Outline each blood parasite and name the species.
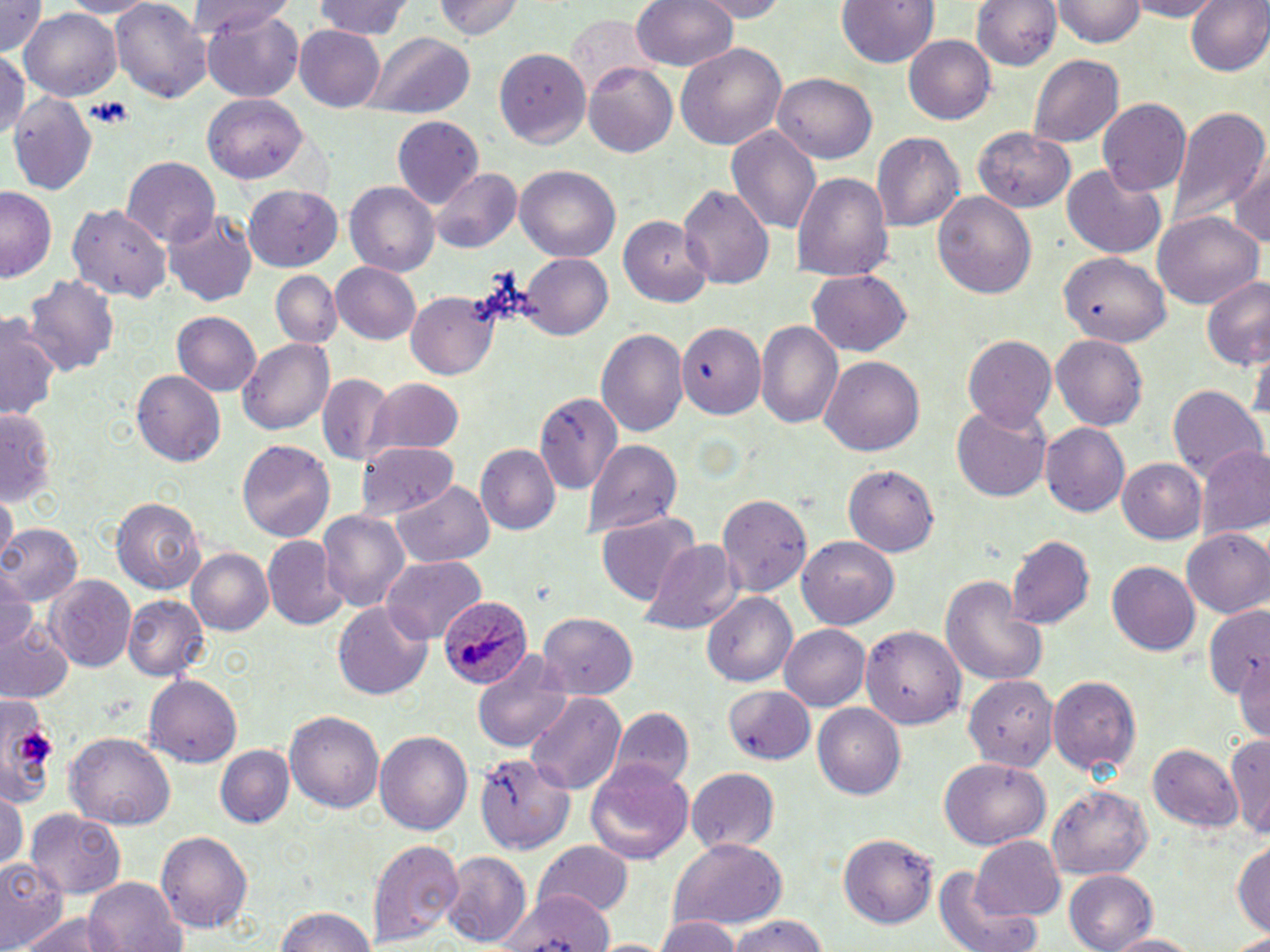

Approximate bounding boxes as named x1/y1/x2/y2 corners in pixels.
Plasmodium ovale-infected red blood cells: (x1=437, y1=598, x2=531, y2=691).
No Plasmodium falciparum, Plasmodium malariae, Plasmodium vivax, Babesia divergens, or Trypanosoma brucei observed.

slide-level diagnosis = Plasmodium ovale
modality = light microscopy
stain = May-Grünwald-Giemsa
platelet locations = approximate bounding boxes as named x1/y1/x2/y2 corners in pixels: (x1=83, y1=98, x2=133, y2=127), (x1=18, y1=729, x2=57, y2=764)
field of view = single
uninfected red blood cell locations = approximate bounding boxes as named x1/y1/x2/y2 corners in pixels: (x1=1, y1=0, x2=49, y2=57), (x1=111, y1=0, x2=214, y2=104), (x1=314, y1=0, x2=417, y2=40), (x1=431, y1=0, x2=522, y2=42), (x1=631, y1=0, x2=739, y2=73), (x1=690, y1=0, x2=794, y2=20), (x1=969, y1=0, x2=1062, y2=71), (x1=1055, y1=0, x2=1145, y2=47), (x1=1125, y1=0, x2=1220, y2=20), (x1=1185, y1=0, x2=1270, y2=79), (x1=836, y1=1, x2=940, y2=69), (x1=187, y1=3, x2=298, y2=44), (x1=202, y1=6, x2=304, y2=102), (x1=19, y1=9, x2=121, y2=103), (x1=563, y1=16, x2=654, y2=101), (x1=295, y1=26, x2=385, y2=110), (x1=366, y1=33, x2=473, y2=120), (x1=904, y1=37, x2=996, y2=123), (x1=677, y1=41, x2=787, y2=151), (x1=494, y1=47, x2=593, y2=146), (x1=1028, y1=52, x2=1124, y2=148), (x1=0, y1=53, x2=28, y2=137), (x1=582, y1=62, x2=678, y2=156), (x1=771, y1=74, x2=877, y2=164), (x1=8, y1=91, x2=100, y2=199), (x1=205, y1=95, x2=307, y2=182), (x1=1097, y1=97, x2=1192, y2=196), (x1=1167, y1=105, x2=1268, y2=230), (x1=391, y1=115, x2=484, y2=212), (x1=973, y1=127, x2=1074, y2=213), (x1=726, y1=128, x2=822, y2=237), (x1=872, y1=130, x2=964, y2=232), (x1=1228, y1=154, x2=1270, y2=250), (x1=122, y1=156, x2=217, y2=245), (x1=1061, y1=164, x2=1168, y2=259), (x1=515, y1=166, x2=620, y2=262), (x1=430, y1=168, x2=522, y2=254), (x1=791, y1=171, x2=892, y2=282), (x1=344, y1=182, x2=438, y2=277), (x1=245, y1=184, x2=343, y2=271), (x1=678, y1=184, x2=774, y2=291), (x1=1, y1=188, x2=55, y2=282), (x1=932, y1=191, x2=1036, y2=299), (x1=69, y1=202, x2=172, y2=304), (x1=165, y1=210, x2=256, y2=307), (x1=620, y1=214, x2=713, y2=305), (x1=1155, y1=214, x2=1262, y2=309), (x1=520, y1=253, x2=613, y2=339), (x1=1060, y1=253, x2=1169, y2=342), (x1=330, y1=262, x2=422, y2=344), (x1=807, y1=268, x2=911, y2=356), (x1=25, y1=271, x2=120, y2=380), (x1=273, y1=271, x2=340, y2=346), (x1=1200, y1=274, x2=1269, y2=371), (x1=408, y1=294, x2=496, y2=377), (x1=1, y1=312, x2=59, y2=423), (x1=170, y1=312, x2=261, y2=398), (x1=757, y1=321, x2=844, y2=430), (x1=678, y1=323, x2=765, y2=421), (x1=597, y1=327, x2=688, y2=436), (x1=962, y1=333, x2=1057, y2=430), (x1=1050, y1=335, x2=1148, y2=430), (x1=237, y1=337, x2=336, y2=435), (x1=820, y1=354, x2=926, y2=458), (x1=132, y1=371, x2=226, y2=466), (x1=317, y1=372, x2=391, y2=467), (x1=369, y1=379, x2=465, y2=456), (x1=1166, y1=382, x2=1266, y2=485), (x1=534, y1=387, x2=624, y2=493), (x1=953, y1=406, x2=1051, y2=502), (x1=0, y1=407, x2=55, y2=507), (x1=1041, y1=423, x2=1130, y2=518), (x1=237, y1=439, x2=335, y2=543), (x1=584, y1=441, x2=681, y2=539), (x1=356, y1=442, x2=460, y2=521), (x1=1196, y1=443, x2=1270, y2=539), (x1=474, y1=444, x2=559, y2=536), (x1=1118, y1=458, x2=1208, y2=545), (x1=842, y1=463, x2=941, y2=557), (x1=393, y1=483, x2=494, y2=566), (x1=716, y1=491, x2=814, y2=596), (x1=2, y1=494, x2=17, y2=558), (x1=112, y1=495, x2=206, y2=594), (x1=318, y1=509, x2=410, y2=611), (x1=596, y1=511, x2=701, y2=607), (x1=0, y1=524, x2=82, y2=606), (x1=1182, y1=529, x2=1270, y2=617), (x1=263, y1=535, x2=347, y2=629), (x1=1006, y1=535, x2=1095, y2=629), (x1=641, y1=536, x2=740, y2=632), (x1=799, y1=536, x2=899, y2=632), (x1=187, y1=548, x2=272, y2=635), (x1=381, y1=556, x2=485, y2=643), (x1=1107, y1=562, x2=1199, y2=657), (x1=0, y1=570, x2=37, y2=652), (x1=941, y1=572, x2=1047, y2=690), (x1=46, y1=576, x2=136, y2=673), (x1=123, y1=594, x2=208, y2=680), (x1=703, y1=594, x2=797, y2=686), (x1=334, y1=602, x2=433, y2=699), (x1=1204, y1=605, x2=1268, y2=710), (x1=540, y1=615, x2=637, y2=697), (x1=0, y1=619, x2=73, y2=703), (x1=858, y1=622, x2=967, y2=727), (x1=779, y1=624, x2=870, y2=711), (x1=472, y1=653, x2=576, y2=752), (x1=1233, y1=654, x2=1269, y2=746), (x1=961, y1=671, x2=1059, y2=776), (x1=143, y1=674, x2=244, y2=768), (x1=1046, y1=674, x2=1141, y2=776), (x1=724, y1=682, x2=814, y2=762), (x1=0, y1=693, x2=60, y2=800), (x1=527, y1=693, x2=625, y2=792), (x1=812, y1=702, x2=906, y2=800), (x1=286, y1=709, x2=385, y2=813), (x1=607, y1=711, x2=694, y2=795), (x1=1226, y1=729, x2=1270, y2=838), (x1=375, y1=730, x2=472, y2=837), (x1=64, y1=733, x2=175, y2=829), (x1=1147, y1=742, x2=1241, y2=831), (x1=217, y1=747, x2=294, y2=828), (x1=475, y1=750, x2=574, y2=854), (x1=584, y1=757, x2=695, y2=865), (x1=939, y1=757, x2=1049, y2=852), (x1=685, y1=767, x2=780, y2=853), (x1=1048, y1=786, x2=1154, y2=878), (x1=0, y1=791, x2=27, y2=874), (x1=24, y1=810, x2=123, y2=895), (x1=156, y1=830, x2=254, y2=934), (x1=836, y1=833, x2=938, y2=929), (x1=970, y1=835, x2=1066, y2=921), (x1=1233, y1=835, x2=1270, y2=939), (x1=368, y1=837, x2=464, y2=945), (x1=669, y1=838, x2=788, y2=931), (x1=535, y1=842, x2=633, y2=920), (x1=444, y1=853, x2=532, y2=945), (x1=0, y1=857, x2=65, y2=948), (x1=926, y1=869, x2=1046, y2=952), (x1=1063, y1=869, x2=1158, y2=951), (x1=83, y1=877, x2=185, y2=951), (x1=498, y1=890, x2=617, y2=952), (x1=273, y1=903, x2=380, y2=952), (x1=13, y1=912, x2=133, y2=952), (x1=655, y1=916, x2=739, y2=952), (x1=725, y1=916, x2=830, y2=952), (x1=1231, y1=930, x2=1270, y2=951), (x1=1104, y1=932, x2=1206, y2=951)
magnification = 1000x
image size = 1270×952 pixels
preparation = thin blood film